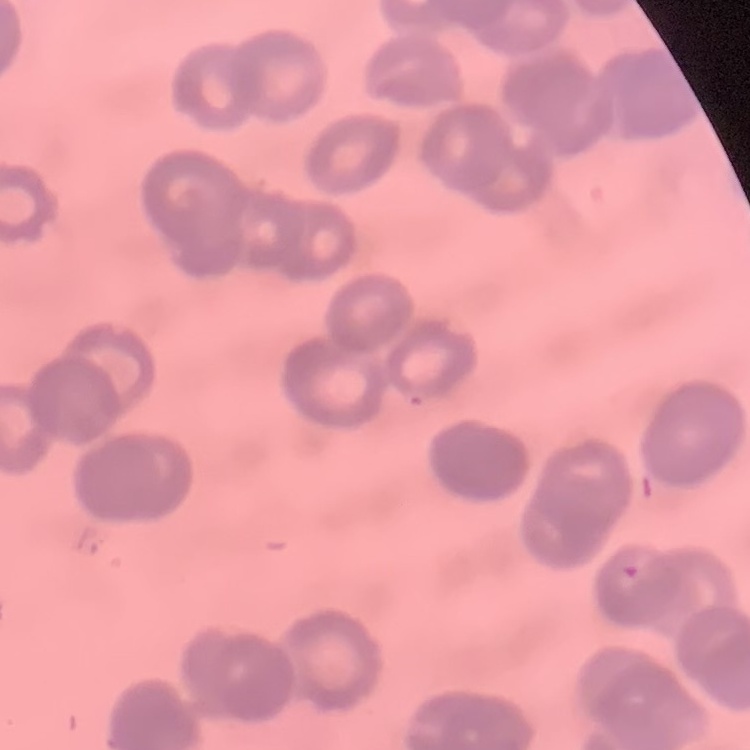
The erythrocytes show rouleaux formation. Stained with either Field's or Giemsa. Square crop of a larger photomicrograph. Thin blood smear.